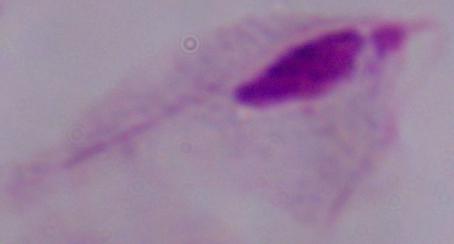

Micrograph. 1000x magnification. A trichomonad is shown.